Locate every uninfected red blood cell.
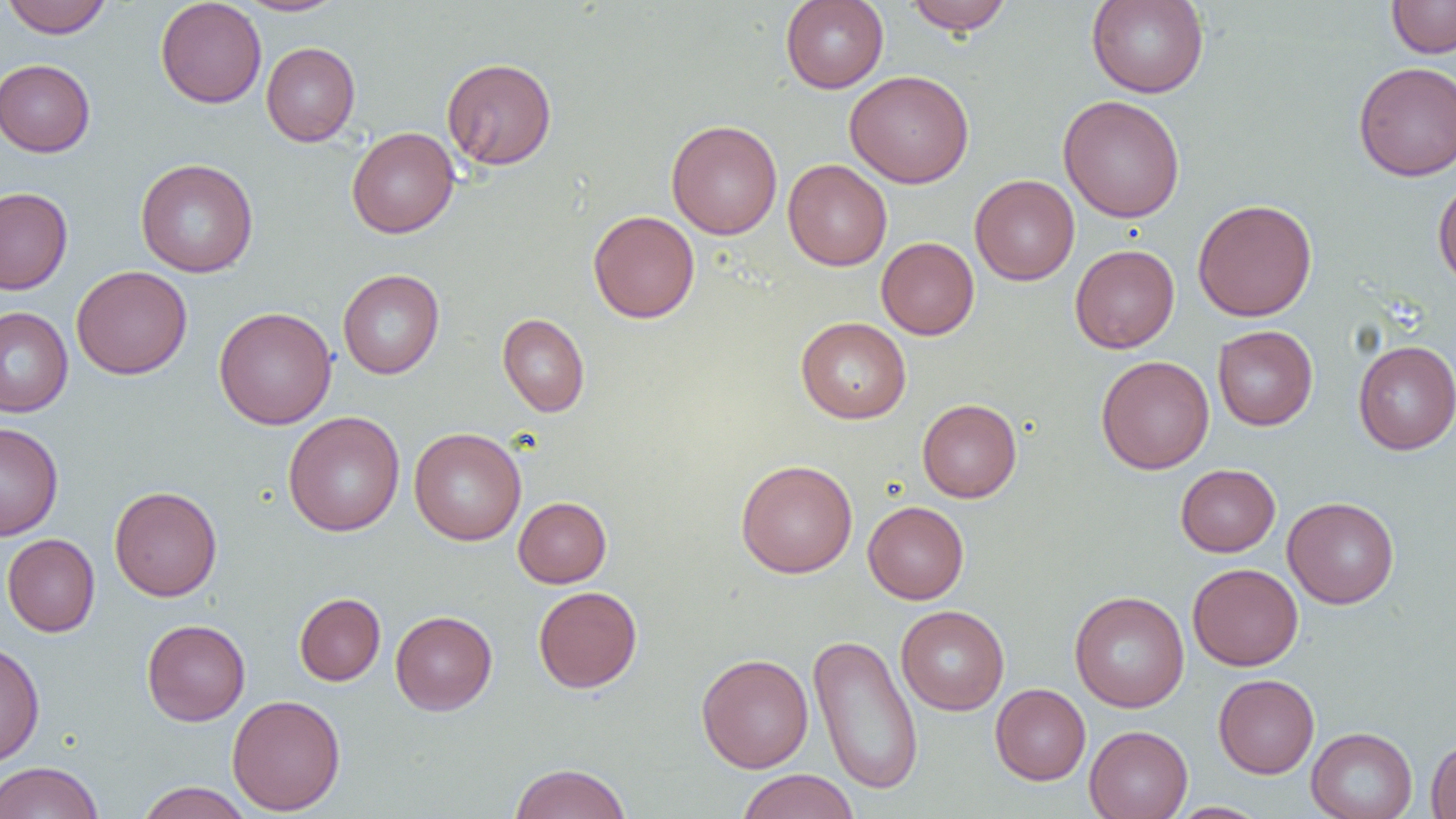

Approximate bounding boxes as [x1, y1, x2, y2] in pixels.
Uninfected red blood cells: [2, 0, 113, 38], [155, 0, 267, 108], [236, 0, 349, 16], [780, 0, 888, 93], [903, 0, 1014, 34], [1086, 0, 1209, 98], [1386, 0, 1456, 58], [261, 42, 360, 146], [441, 57, 557, 170], [0, 59, 95, 157], [1353, 61, 1456, 180], [845, 70, 974, 188], [1058, 95, 1185, 223], [666, 120, 782, 240], [347, 127, 460, 238], [135, 159, 258, 277], [782, 159, 892, 271], [969, 174, 1080, 285], [1433, 177, 1456, 289], [0, 187, 73, 294], [1192, 198, 1318, 322], [588, 210, 700, 323], [876, 237, 979, 340], [1070, 244, 1180, 353], [71, 265, 192, 379], [337, 269, 445, 379], [0, 306, 73, 417], [214, 306, 337, 430], [497, 313, 590, 417], [796, 316, 911, 423], [1213, 325, 1318, 430], [1353, 340, 1456, 454], [1096, 355, 1214, 474], [917, 398, 1021, 502], [283, 411, 405, 537], [0, 422, 64, 540], [409, 427, 527, 545], [735, 459, 857, 578], [1176, 464, 1280, 557], [109, 486, 222, 601], [513, 496, 611, 587], [1282, 496, 1399, 608], [863, 501, 969, 604], [2, 534, 100, 637], [1188, 563, 1303, 670], [533, 586, 642, 693], [1069, 590, 1189, 712], [294, 593, 385, 685], [896, 605, 1009, 715], [390, 610, 497, 715], [141, 619, 250, 725], [808, 633, 923, 795], [0, 640, 45, 767], [696, 653, 813, 772], [1213, 674, 1319, 778], [990, 683, 1090, 785], [226, 694, 346, 815], [1084, 725, 1193, 819], [1306, 727, 1418, 819], [1426, 735, 1456, 819], [0, 761, 104, 819], [508, 762, 632, 819], [736, 769, 860, 819], [135, 782, 254, 819], [1167, 802, 1271, 818].

Summary:
  - Slide-level diagnosis: no evidence of blood parasites
  - Preparation: thin blood film
  - Modality: optical microscopy
  - Magnification: 1000x
  - Field of view: single
  - Image size: 1456×819 pixels